Classify this cell by malaria status.
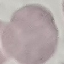

It is uninfected.

Thin blood film. Photographed with a smartphone camera at the microscope eyepiece. Giemsa-stained preparation. Automatically extracted cell patch, resized to 64 × 64 pixels.